Locate and identify every blood parasite.
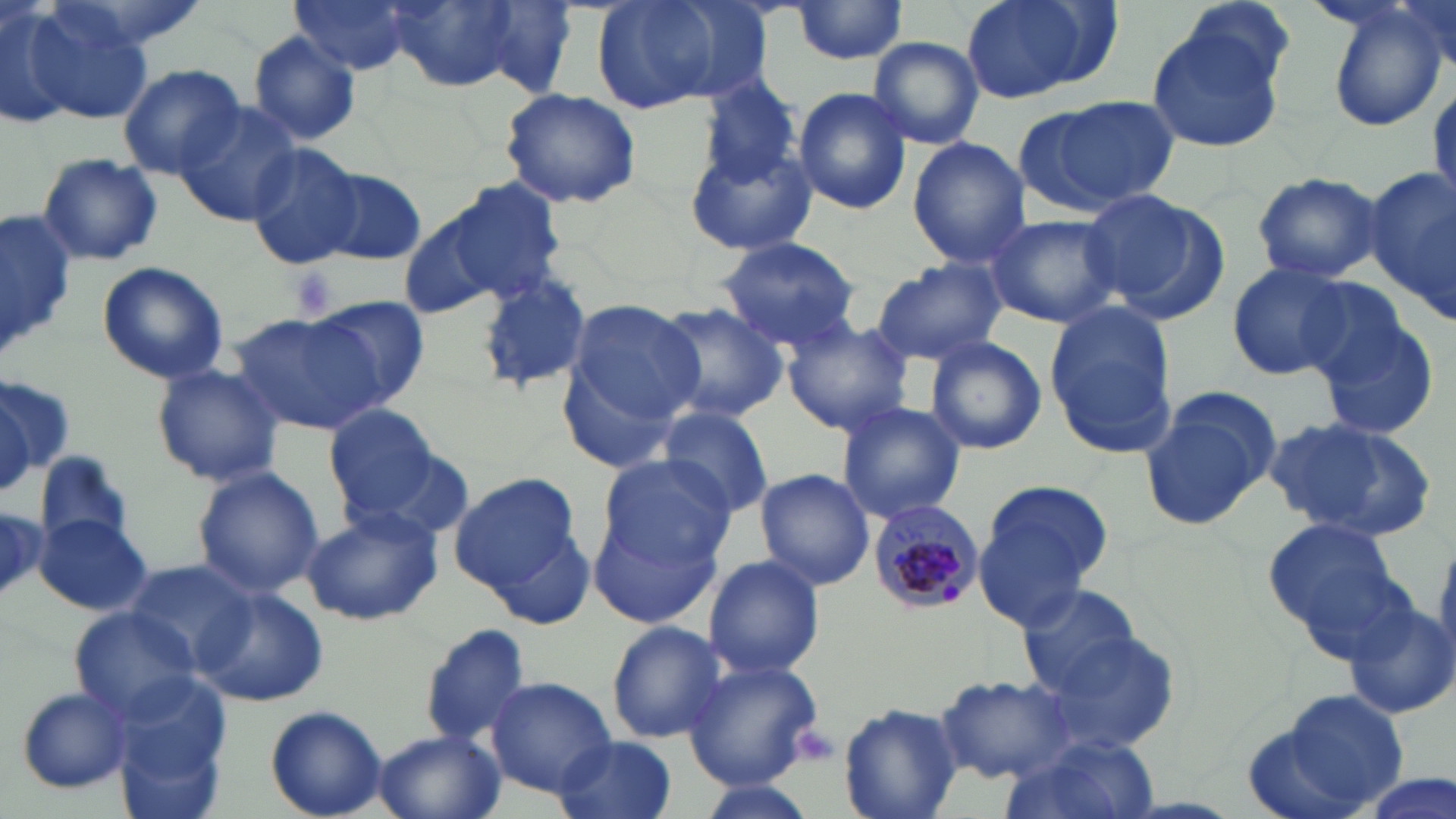
Approximate bounding boxes as named x1/y1/x2/y2 corners in pixels.
Plasmodium malariae-infected red blood cells: (x1=867, y1=500, x2=986, y2=616).
No Plasmodium falciparum, Plasmodium ovale, Plasmodium vivax, Babesia divergens, or Trypanosoma brucei observed.

Summary:
  - Uninfected red blood cell locations: (x1=0, y1=0, x2=74, y2=130), (x1=386, y1=0, x2=519, y2=91), (x1=591, y1=0, x2=764, y2=116), (x1=794, y1=0, x2=910, y2=67), (x1=960, y1=0, x2=1113, y2=104), (x1=1392, y1=0, x2=1453, y2=68), (x1=291, y1=1, x2=412, y2=74), (x1=17, y1=2, x2=156, y2=128), (x1=474, y1=3, x2=581, y2=98), (x1=1325, y1=4, x2=1448, y2=133), (x1=1143, y1=14, x2=1289, y2=156), (x1=245, y1=29, x2=363, y2=146), (x1=868, y1=36, x2=985, y2=148), (x1=117, y1=63, x2=246, y2=178), (x1=694, y1=74, x2=805, y2=197), (x1=1429, y1=86, x2=1456, y2=212), (x1=500, y1=87, x2=643, y2=209), (x1=793, y1=88, x2=913, y2=214), (x1=1016, y1=96, x2=1179, y2=216), (x1=173, y1=100, x2=301, y2=228), (x1=907, y1=138, x2=1029, y2=269), (x1=686, y1=141, x2=817, y2=260), (x1=244, y1=143, x2=367, y2=269), (x1=38, y1=152, x2=162, y2=267), (x1=313, y1=167, x2=428, y2=267), (x1=1366, y1=168, x2=1456, y2=318), (x1=1249, y1=171, x2=1386, y2=282), (x1=429, y1=179, x2=568, y2=305), (x1=1082, y1=188, x2=1222, y2=315), (x1=398, y1=203, x2=527, y2=322), (x1=0, y1=206, x2=77, y2=362), (x1=984, y1=212, x2=1120, y2=329), (x1=718, y1=236, x2=865, y2=351), (x1=97, y1=261, x2=229, y2=384), (x1=871, y1=261, x2=1004, y2=365), (x1=1226, y1=261, x2=1356, y2=381), (x1=475, y1=270, x2=593, y2=395), (x1=1293, y1=275, x2=1415, y2=389), (x1=312, y1=295, x2=432, y2=410), (x1=562, y1=297, x2=704, y2=430), (x1=651, y1=302, x2=788, y2=424), (x1=1045, y1=304, x2=1176, y2=457), (x1=227, y1=313, x2=387, y2=436), (x1=1314, y1=313, x2=1441, y2=439), (x1=780, y1=321, x2=913, y2=434), (x1=924, y1=337, x2=1048, y2=456), (x1=152, y1=363, x2=284, y2=487), (x1=0, y1=381, x2=62, y2=489), (x1=1138, y1=391, x2=1278, y2=531), (x1=834, y1=400, x2=966, y2=524), (x1=323, y1=404, x2=445, y2=522), (x1=656, y1=404, x2=774, y2=518), (x1=1263, y1=414, x2=1437, y2=540), (x1=355, y1=442, x2=475, y2=547), (x1=34, y1=448, x2=135, y2=556), (x1=595, y1=451, x2=736, y2=569), (x1=191, y1=467, x2=325, y2=600), (x1=753, y1=468, x2=875, y2=590), (x1=450, y1=472, x2=583, y2=597), (x1=977, y1=479, x2=1113, y2=613), (x1=587, y1=498, x2=726, y2=632), (x1=299, y1=504, x2=444, y2=626), (x1=0, y1=506, x2=46, y2=598), (x1=35, y1=514, x2=152, y2=615), (x1=1262, y1=515, x2=1402, y2=644), (x1=702, y1=553, x2=826, y2=679), (x1=124, y1=558, x2=256, y2=669), (x1=193, y1=585, x2=329, y2=706), (x1=1017, y1=585, x2=1146, y2=700), (x1=1342, y1=599, x2=1456, y2=722), (x1=69, y1=610, x2=201, y2=721), (x1=606, y1=620, x2=728, y2=744), (x1=418, y1=622, x2=535, y2=748), (x1=1033, y1=628, x2=1184, y2=758), (x1=684, y1=658, x2=825, y2=790), (x1=937, y1=673, x2=1078, y2=782), (x1=114, y1=677, x2=230, y2=817), (x1=486, y1=678, x2=616, y2=796), (x1=11, y1=684, x2=135, y2=795), (x1=1247, y1=689, x2=1412, y2=819), (x1=840, y1=702, x2=962, y2=819), (x1=265, y1=705, x2=387, y2=818), (x1=370, y1=729, x2=506, y2=819), (x1=553, y1=734, x2=679, y2=819), (x1=997, y1=739, x2=1161, y2=819), (x1=1352, y1=771, x2=1454, y2=819)
  - Platelet locations: (x1=286, y1=265, x2=338, y2=322), (x1=788, y1=720, x2=842, y2=769)
  - Slide-level diagnosis: Plasmodium malariae
  - Magnification: 1000x
  - Field of view: one of a larger specimen
  - Preparation: thin blood film
  - Image size: 1456×819 pixels
  - Modality: light microscopy
  - Stain: May-Grünwald-Giemsa